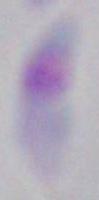

Summary:
  - Magnification: 1000x
  - Identification: Toxoplasma gondii
  - Modality: photomicrograph